Report the malaria status of this cell.
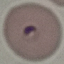
Parasitized.

{
  "capture": "smartphone through the microscope eyepiece",
  "image_type": "cell patch, automatically extracted from a larger field of view and resized to 64 × 64 pixels",
  "stain": "Giemsa",
  "preparation": "thin smear"
}